Classify this cell by malaria status.
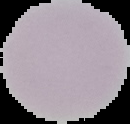

Uninfected.

image type = cell region segmented out of the field of view; surrounding area masked to black
preparation = thin blood smear
image size = 130×124 pixels